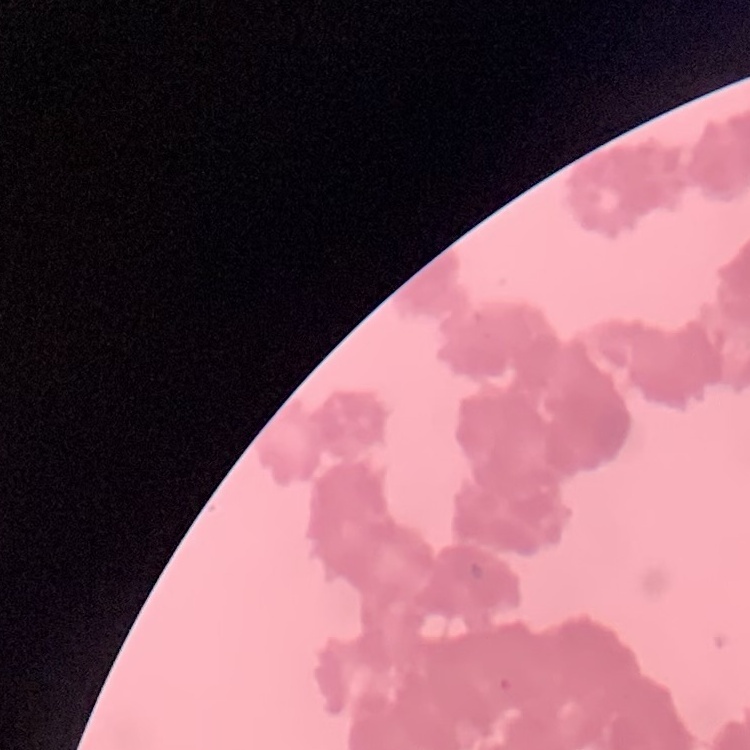 The erythrocytes exhibit rouleaux formation. Thin blood smear. Stained with either Field's or Giemsa. One tile cut from a larger photomicrograph.